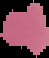
Summary:
  - Result: no Plasmodium parasites detected
  - Preparation: thin blood film
  - Image type: cell region segmented out of the field of view; surrounding area masked to black
  - Image size: 49×58 pixels